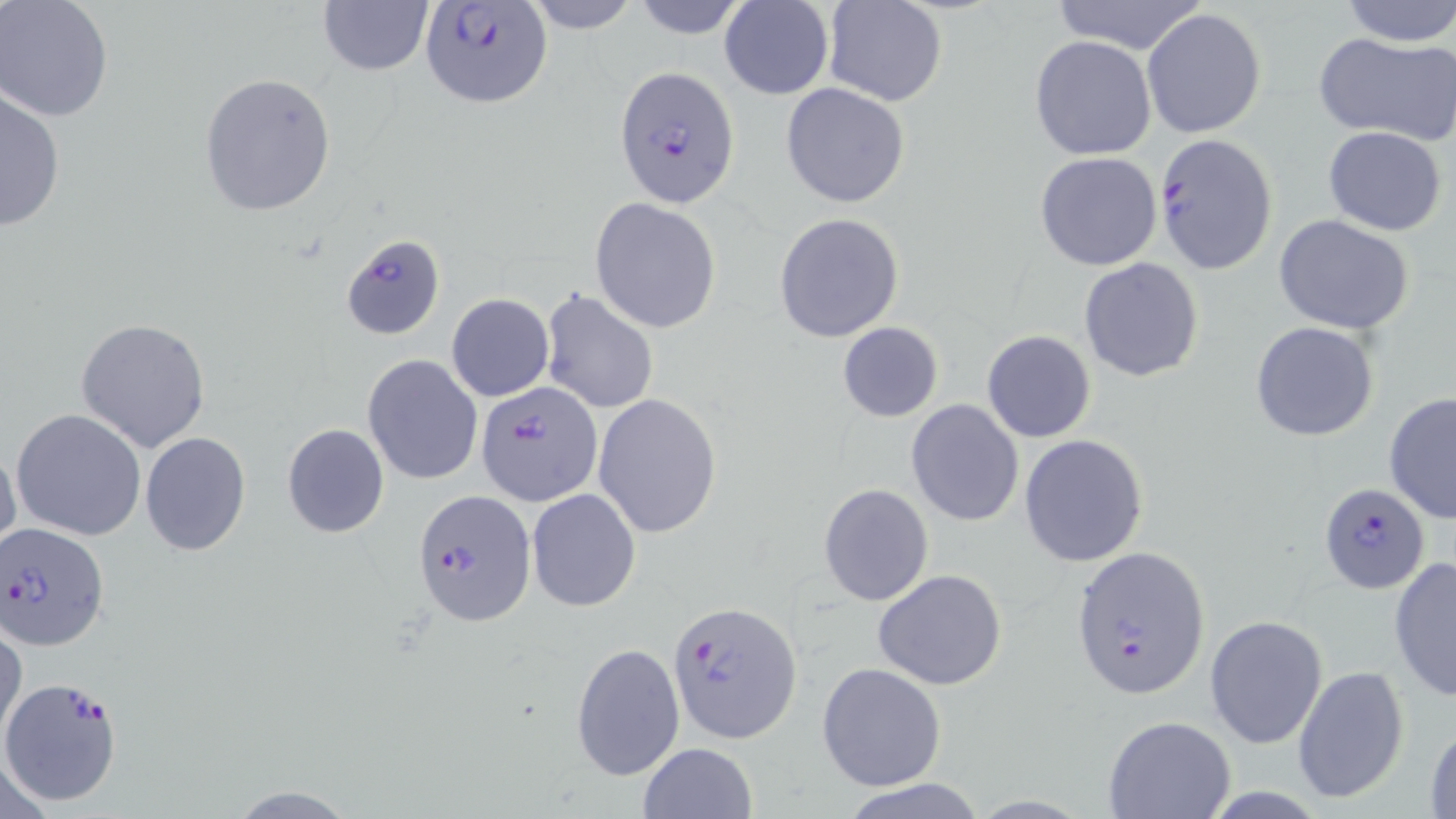

slide-level diagnosis = Plasmodium falciparum
magnification = 1000x
field of view = one of a larger specimen
uninfected red blood cell locations = approximate bounding boxes as (x1, y1, x2, y2) in pixels: (522, 0, 643, 33), (629, 0, 751, 40), (1341, 0, 1456, 47), (0, 1, 116, 121), (317, 1, 433, 77), (718, 1, 834, 99), (824, 1, 946, 106), (1049, 1, 1210, 55), (1142, 8, 1267, 141), (1314, 32, 1456, 146), (1030, 36, 1156, 160), (198, 72, 337, 218), (781, 83, 910, 208), (0, 85, 67, 235), (1324, 126, 1448, 236), (1034, 152, 1163, 271), (591, 198, 722, 333), (774, 212, 905, 342), (1274, 214, 1417, 335), (1078, 257, 1204, 383), (539, 288, 660, 415), (445, 293, 554, 402), (76, 317, 211, 453), (1249, 321, 1381, 442), (836, 323, 944, 421), (982, 330, 1096, 443), (363, 354, 484, 485), (1383, 390, 1456, 525), (593, 392, 723, 539), (906, 400, 1024, 527), (12, 408, 147, 541), (282, 423, 390, 538), (139, 431, 252, 556), (1019, 434, 1149, 567), (0, 443, 23, 561), (818, 482, 933, 606), (526, 487, 641, 612), (1388, 555, 1456, 703), (872, 569, 1007, 691), (1205, 614, 1328, 747), (1, 624, 25, 748), (570, 642, 685, 781), (816, 663, 946, 790), (1291, 665, 1410, 804), (1102, 715, 1237, 819), (1424, 720, 1456, 819), (638, 741, 759, 819), (834, 778, 992, 818)
Plasmodium falciparum-infected red blood cell locations = approximate bounding boxes as (x1, y1, x2, y2) in pixels: (416, 2, 553, 110), (614, 65, 738, 210), (1153, 132, 1278, 273), (339, 232, 446, 340), (475, 379, 601, 505), (1320, 483, 1430, 592), (413, 490, 537, 628), (0, 521, 108, 651), (1071, 546, 1211, 696), (669, 602, 802, 744), (1, 676, 124, 806)
stain = May-Grünwald-Giemsa
image size = 1456×819 pixels
preparation = thin blood film
modality = optical microscopy